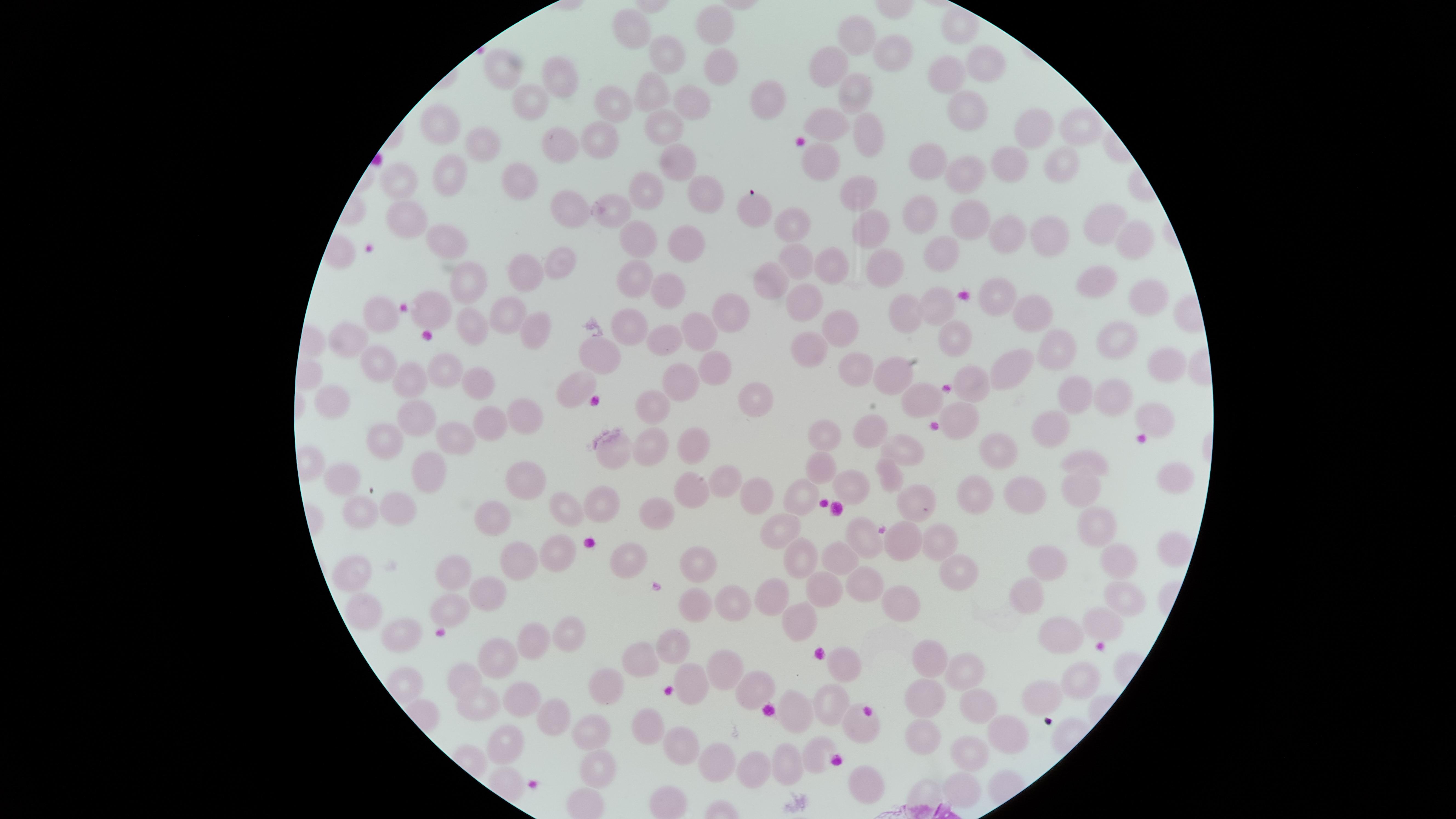

Approximate marker points, in pixels from the top-left corner. Uninfected red blood cells: (x=635, y=26), (x=715, y=27), (x=951, y=27), (x=856, y=34), (x=892, y=51), (x=668, y=53), (x=980, y=63), (x=721, y=64), (x=834, y=65), (x=501, y=67), (x=953, y=72), (x=561, y=76), (x=854, y=90), (x=653, y=94), (x=767, y=94), (x=615, y=100), (x=699, y=101), (x=530, y=102), (x=964, y=109), (x=828, y=123), (x=446, y=125), (x=662, y=125), (x=1030, y=129), (x=1074, y=130), (x=865, y=131), (x=561, y=140), (x=600, y=141), (x=485, y=142), (x=1057, y=154), (x=827, y=156), (x=682, y=160), (x=927, y=161), (x=1009, y=163), (x=965, y=174), (x=453, y=178), (x=400, y=183), (x=521, y=186), (x=856, y=191), (x=646, y=192), (x=706, y=192), (x=570, y=203), (x=752, y=208), (x=407, y=210), (x=612, y=213), (x=920, y=215), (x=1099, y=218), (x=788, y=220), (x=968, y=220), (x=868, y=228), (x=1008, y=230), (x=635, y=233), (x=1051, y=233), (x=1140, y=238), (x=447, y=242), (x=689, y=242), (x=942, y=254), (x=828, y=257), (x=803, y=261), (x=882, y=262), (x=557, y=266), (x=526, y=274), (x=637, y=278), (x=770, y=278), (x=463, y=279), (x=668, y=279), (x=1099, y=286), (x=809, y=300), (x=996, y=300), (x=1143, y=301), (x=941, y=307), (x=433, y=310), (x=385, y=312), (x=736, y=312), (x=912, y=312), (x=506, y=314), (x=1034, y=314), (x=467, y=322), (x=530, y=326), (x=628, y=327), (x=841, y=327), (x=705, y=331), (x=666, y=334), (x=947, y=337), (x=347, y=339), (x=1115, y=347), (x=1064, y=349), (x=806, y=350), (x=599, y=353), (x=377, y=362), (x=1162, y=362), (x=709, y=364), (x=1001, y=364), (x=446, y=367), (x=847, y=369), (x=889, y=369), (x=683, y=373), (x=406, y=376), (x=469, y=376), (x=973, y=378), (x=580, y=387), (x=1074, y=393), (x=1115, y=393), (x=339, y=395), (x=921, y=398), (x=755, y=399), (x=515, y=407), (x=646, y=416), (x=1158, y=416), (x=421, y=417), (x=964, y=419), (x=485, y=421), (x=871, y=427), (x=1052, y=431), (x=826, y=432), (x=385, y=437), (x=452, y=439), (x=650, y=444), (x=691, y=444), (x=909, y=445), (x=615, y=450), (x=1002, y=451), (x=1088, y=458), (x=813, y=460), (x=887, y=476), (x=1168, y=476), (x=420, y=477), (x=347, y=478), (x=727, y=485), (x=528, y=487), (x=1081, y=487), (x=851, y=490), (x=978, y=491), (x=915, y=492), (x=694, y=496), (x=757, y=497), (x=599, y=500), (x=799, y=500), (x=1033, y=500), (x=569, y=508), (x=363, y=512), (x=401, y=512), (x=657, y=515), (x=496, y=519), (x=1095, y=525), (x=784, y=529), (x=938, y=534), (x=859, y=537), (x=903, y=544), (x=1167, y=551), (x=803, y=553), (x=836, y=553), (x=560, y=555), (x=629, y=561), (x=1117, y=561), (x=706, y=563), (x=1050, y=563), (x=958, y=566), (x=515, y=569), (x=453, y=575), (x=355, y=576), (x=872, y=584), (x=821, y=590), (x=1027, y=593), (x=1121, y=593), (x=486, y=594), (x=903, y=596), (x=775, y=599), (x=729, y=600), (x=695, y=605), (x=360, y=612), (x=453, y=613), (x=804, y=617), (x=1103, y=621), (x=568, y=630), (x=1059, y=634), (x=405, y=638), (x=530, y=640), (x=678, y=640), (x=643, y=653), (x=493, y=654), (x=930, y=654), (x=727, y=662), (x=841, y=664), (x=469, y=674), (x=958, y=674), (x=1083, y=676), (x=694, y=684), (x=601, y=685), (x=749, y=688), (x=1046, y=694), (x=927, y=697), (x=521, y=699), (x=977, y=706), (x=828, y=707), (x=480, y=710), (x=796, y=713), (x=546, y=717), (x=646, y=724), (x=854, y=726), (x=1007, y=729), (x=592, y=732), (x=925, y=737), (x=510, y=740), (x=683, y=741), (x=818, y=752), (x=969, y=752), (x=714, y=762), (x=785, y=763), (x=760, y=767), (x=599, y=775), (x=863, y=781), (x=960, y=788), (x=927, y=789). Photographed with a smartphone camera through the microscope eyepiece. Giemsa stain. Presence: no malaria parasites detected. One field of view of the specimen. The visible region is circular. Thin blood film. Image is 1456×819 pixels.